Identify the parasite.
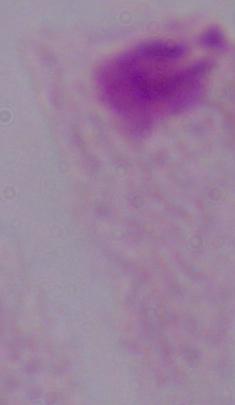
A trichomonad.

Captured at 1000x magnification. Photomicrograph.